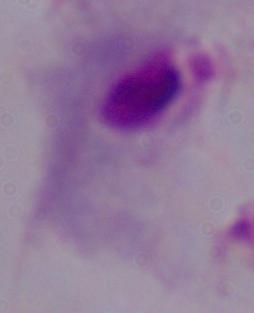
Summary:
  - Magnification: 1000x
  - Modality: micrograph
  - Identification: trichomonad